Point out each leukocyte.
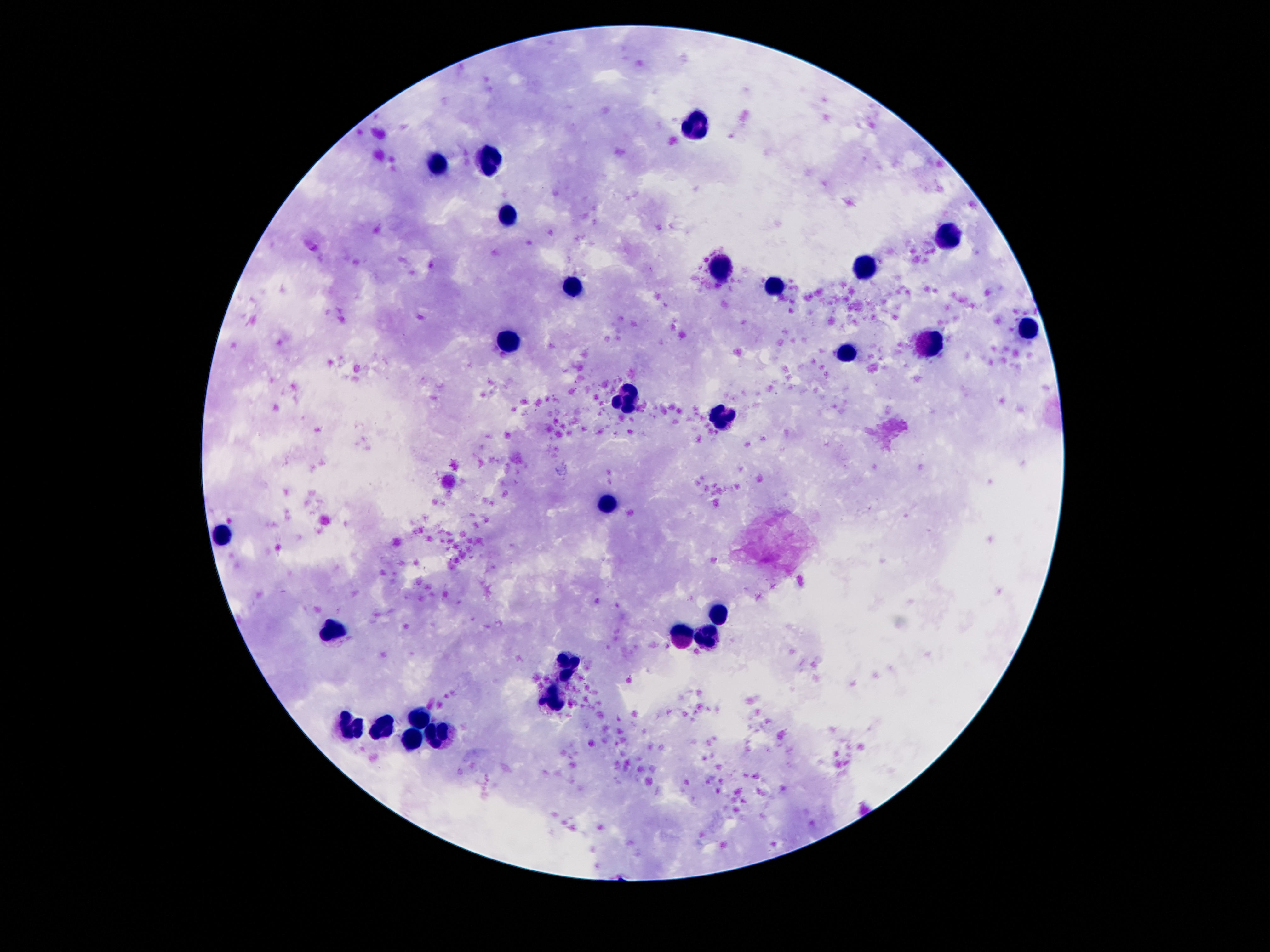

Approximate centers as {x, y} in pixels.
Leukocytes: {692, 123}, {489, 161}, {438, 165}, {507, 216}, {949, 236}, {867, 266}, {726, 268}, {571, 282}, {776, 284}, {1029, 328}, {934, 342}, {511, 346}, {847, 355}, {628, 399}, {721, 417}, {611, 506}, {221, 530}, {717, 611}, {336, 631}, {684, 635}, {710, 640}, {566, 664}, {551, 699}, {420, 717}, {352, 727}, {378, 728}, {440, 736}, {409, 741}.

Summary:
  - Image size: 1270×952 pixels
  - Magnification: 100x
  - Stain: Giemsa
  - Capture: smartphone camera through the microscope eyepiece
  - Field of view: single
  - Patient malaria status: uninfected
  - Preparation: thick blood smear